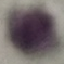
result = no malaria parasites detected
preparation = thin smear
image type = automatically extracted cell patch, resized to 64 × 64 pixels
stain = Giemsa
capture = smartphone camera at the microscope eyepiece